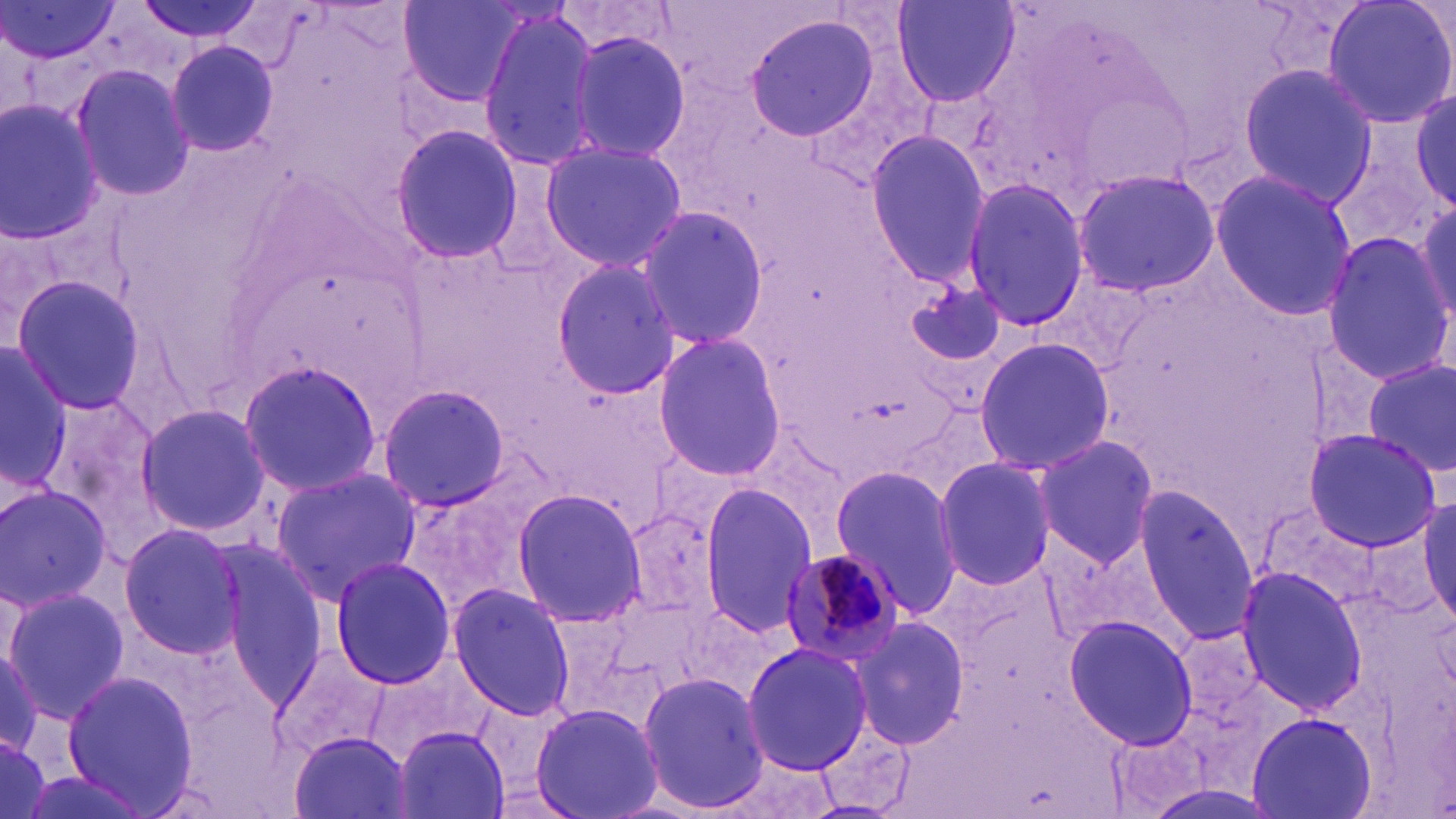
slide-level diagnosis = Plasmodium malariae
image size = 1456×819 pixels
preparation = thin blood film
modality = light microscopy
field of view = one of a larger specimen
stain = May-Grünwald-Giemsa
Plasmodium malariae-infected red blood cell locations = approximate bounding boxes as [x1, y1, x2, y2] in pixels: [779, 549, 908, 666]
uninfected red blood cell locations = approximate bounding boxes as [x1, y1, x2, y2] in pixels: [136, 0, 266, 43], [397, 0, 531, 105], [894, 0, 1020, 108], [1320, 0, 1456, 131], [1, 2, 121, 64], [475, 7, 603, 176], [740, 11, 884, 143], [564, 26, 695, 167], [164, 41, 280, 157], [71, 62, 193, 201], [1237, 63, 1378, 204], [1412, 88, 1455, 209], [0, 98, 108, 244], [390, 122, 524, 265], [865, 130, 989, 288], [537, 138, 687, 275], [1070, 168, 1219, 298], [1208, 170, 1357, 321], [960, 179, 1093, 332], [1413, 196, 1454, 330], [635, 205, 772, 350], [1320, 233, 1454, 383], [550, 260, 683, 398], [8, 273, 150, 417], [903, 276, 1013, 374], [650, 332, 788, 478], [975, 336, 1113, 475], [1, 337, 69, 495], [237, 358, 383, 499], [1362, 360, 1456, 481], [375, 383, 512, 513], [34, 389, 170, 546], [133, 404, 269, 537], [1305, 428, 1439, 551], [1032, 432, 1161, 570], [932, 456, 1058, 590], [828, 463, 966, 618], [270, 467, 420, 603], [0, 480, 113, 610], [698, 484, 823, 635], [1135, 485, 1259, 646], [510, 487, 646, 629], [1419, 494, 1455, 625], [113, 525, 248, 662], [327, 557, 455, 687], [1234, 566, 1366, 715], [447, 584, 576, 720], [1, 585, 128, 722], [1064, 615, 1199, 749], [852, 616, 970, 750], [739, 641, 874, 776], [0, 646, 45, 761], [60, 668, 199, 814], [635, 670, 771, 816], [530, 702, 664, 819], [1246, 712, 1377, 819], [391, 726, 510, 818], [0, 731, 51, 819], [290, 731, 413, 818], [714, 748, 845, 818]
magnification = 1000x